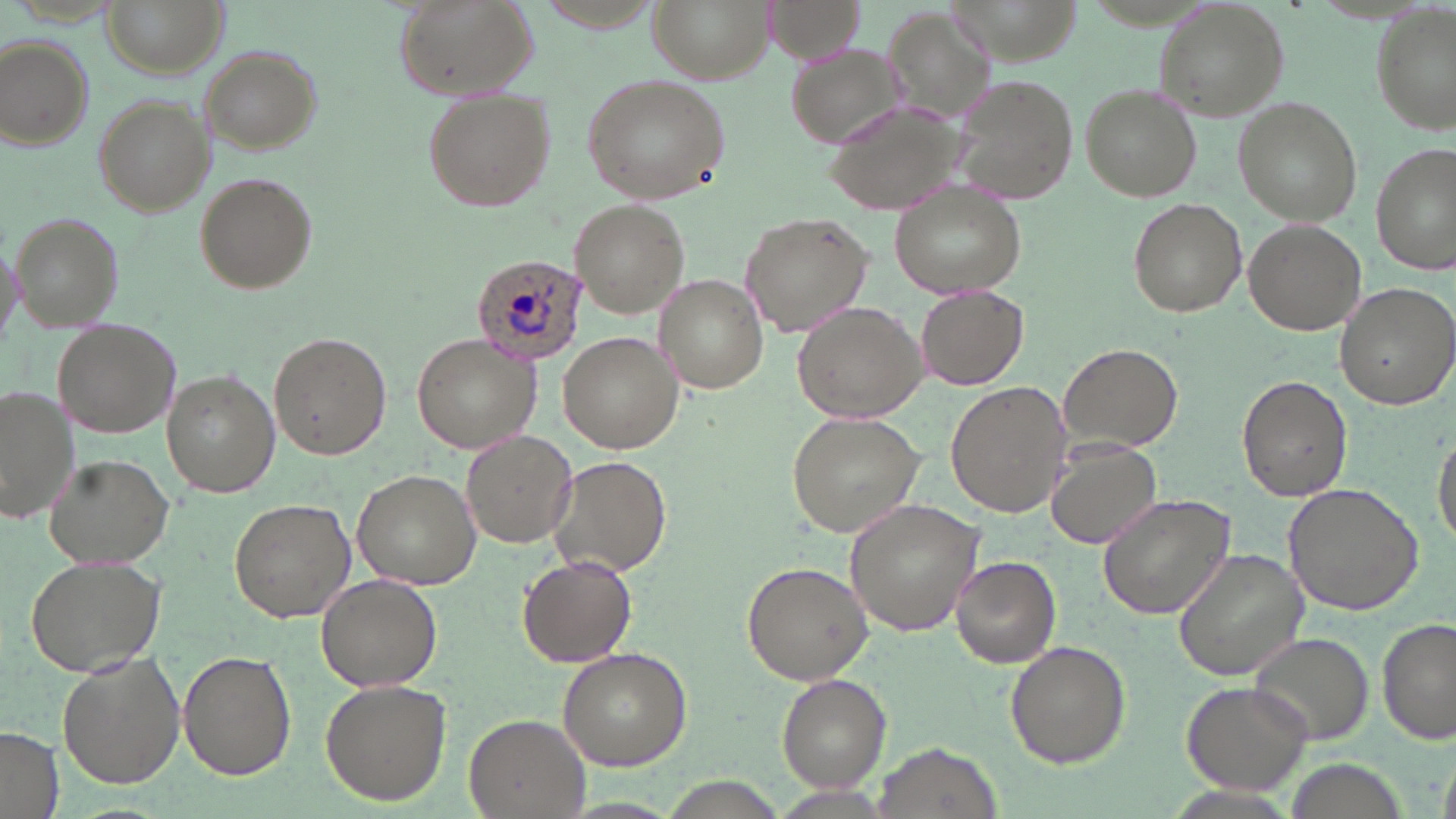

slide-level diagnosis = Plasmodium ovale
stain = May-Grünwald-Giemsa
preparation = thin blood smear
image size = 1456×819 pixels
Plasmodium ovale-infected red blood cell locations = approximate bounding boxes as (x1,y1)-(x2,y2) corner pairs in pixels: (471,250)-(589,363)
uninfected red blood cell locations = approximate bounding boxes as (x1,y1)-(x2,y2) corner pairs in pixels: (102,0)-(224,77), (392,0)-(538,101), (650,0)-(773,83), (761,1)-(864,63), (1153,2)-(1289,117), (884,8)-(1006,125), (1372,8)-(1455,134), (2,34)-(95,151), (785,40)-(910,148), (198,45)-(323,155), (577,72)-(733,207), (948,75)-(1076,207), (1078,84)-(1201,201), (423,89)-(552,211), (92,93)-(214,216), (821,94)-(968,218), (1233,98)-(1362,226), (1370,140)-(1454,276), (195,172)-(317,293), (889,180)-(1026,296), (1127,199)-(1248,316), (570,200)-(692,317), (10,211)-(122,331), (739,212)-(875,336), (1242,217)-(1366,334), (0,231)-(25,343), (655,275)-(768,392), (1337,281)-(1456,409), (915,284)-(1028,390), (792,299)-(929,423), (55,320)-(180,439), (269,331)-(392,461), (558,333)-(684,454), (412,334)-(543,454), (1060,342)-(1181,454), (162,370)-(280,499), (1238,374)-(1353,503), (945,381)-(1073,518), (0,384)-(78,528), (784,410)-(924,539), (1433,424)-(1456,554), (461,430)-(577,547), (1045,440)-(1165,549), (44,453)-(175,571), (548,454)-(671,579), (353,468)-(480,588), (1285,480)-(1427,617), (1097,493)-(1238,621), (844,496)-(988,636), (229,498)-(356,622), (1170,548)-(1310,683), (24,552)-(167,678), (518,555)-(637,666), (950,555)-(1062,668), (740,559)-(873,685), (316,574)-(441,692), (1378,617)-(1454,744), (1247,631)-(1374,746), (1004,640)-(1130,768), (557,645)-(695,770), (178,649)-(297,781), (58,653)-(186,789), (775,673)-(889,790), (320,678)-(452,806), (1180,678)-(1315,798), (464,712)-(590,818), (0,725)-(63,819), (876,739)-(1003,817)
modality = light microscopy
field of view = single
magnification = 1000x